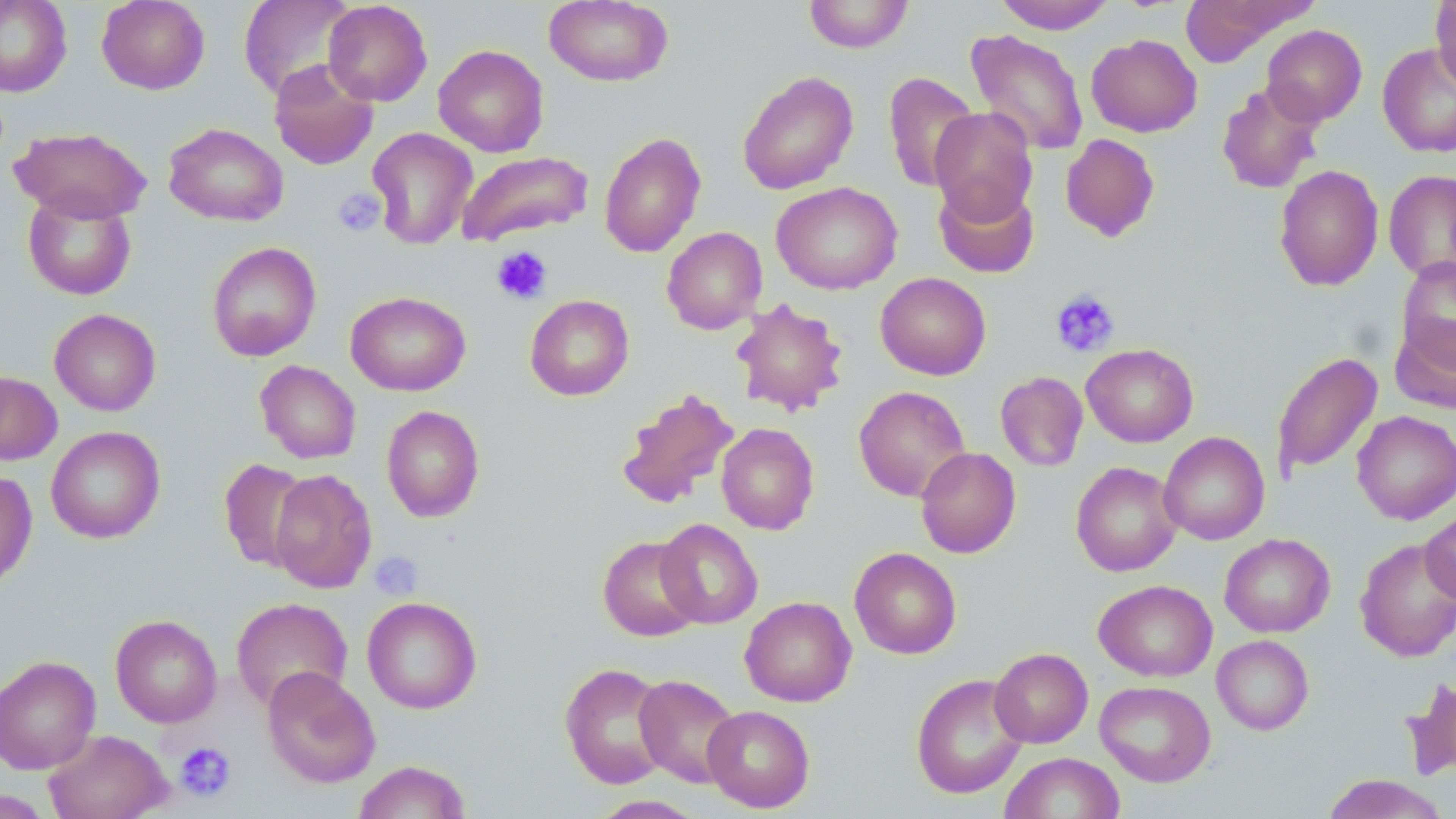

slide_level_diagnosis: no evidence of blood parasites
uninfected_red_blood_cell_locations: 'approximate bounding boxes as (x1,y1)-(x2,y2) corner pairs in pixels: (0,0)-(72,97), (96,0)-(210,94), (238,0)-(357,100), (544,0)-(673,87), (803,0)-(914,53), (994,0)-(1115,34), (1430,0)-(1456,92), (322,1)-(432,106), (1179,2)-(1310,67), (1261,25)-(1367,126), (965,29)-(1089,156), (1085,34)-(1202,137), (1377,42)-(1456,158), (433,44)-(549,157), (269,60)-(379,170), (737,70)-(859,195), (883,71)-(980,192), (1216,81)-(1324,194), (929,107)-(1038,224), (163,122)-(289,227), (11,127)-(151,223), (367,127)-(477,249), (598,132)-(706,258), (1060,133)-(1160,242), (456,150)-(594,246), (1273,164)-(1383,292), (1383,169)-(1456,281), (933,180)-(1040,278), (772,181)-(902,295), (22,191)-(137,301), (662,226)-(767,334), (207,241)-(321,361), (1396,256)-(1456,368), (875,272)-(991,380), (345,291)-(471,396), (525,295)-(634,400), (731,298)-(849,417), (49,308)-(161,416), (1390,317)-(1456,413), (1081,343)-(1198,447), (1271,351)-(1383,478), (255,360)-(361,464), (0,370)-(62,465), (995,371)-(1088,471), (854,385)-(971,502), (615,388)-(740,510), (382,405)-(485,523), (1352,410)-(1456,524), (716,422)-(819,534), (45,426)-(165,543), (1158,431)-(1270,545), (915,447)-(1021,558), (218,458)-(312,572), (1071,461)-(1182,577), (269,468)-(377,593), (0,470)-(37,591), (1420,508)-(1455,605), (655,518)-(763,629), (1219,533)-(1335,637), (597,536)-(704,642), (1354,537)-(1456,662), (849,547)-(962,659), (1094,579)-(1217,681), (362,596)-(483,714), (740,596)-(856,707), (231,597)-(353,713), (110,614)-(223,728), (1212,635)-(1313,735), (989,647)-(1093,748), (0,655)-(101,775), (559,662)-(672,789), (262,667)-(380,789), (911,673)-(1029,799), (634,674)-(742,787), (1401,674)-(1456,781), (1095,680)-(1216,787), (702,704)-(815,812), (44,728)-(173,819), (999,752)-(1125,818), (352,760)-(471,819), (1320,774)-(1450,818), (0,790)-(53,818), (588,795)-(708,818)'
field_of_view: single
preparation: thin blood smear
stain: May-Grünwald-Giemsa
platelet_locations: 'approximate bounding boxes as (x1,y1)-(x2,y2) corner pairs in pixels: (334,188)-(386,236), (491,246)-(552,305), (1050,288)-(1120,357), (368,552)-(423,598), (174,741)-(237,802)'
image_size: 1456×819 pixels
modality: optical microscopy
magnification: 1000x